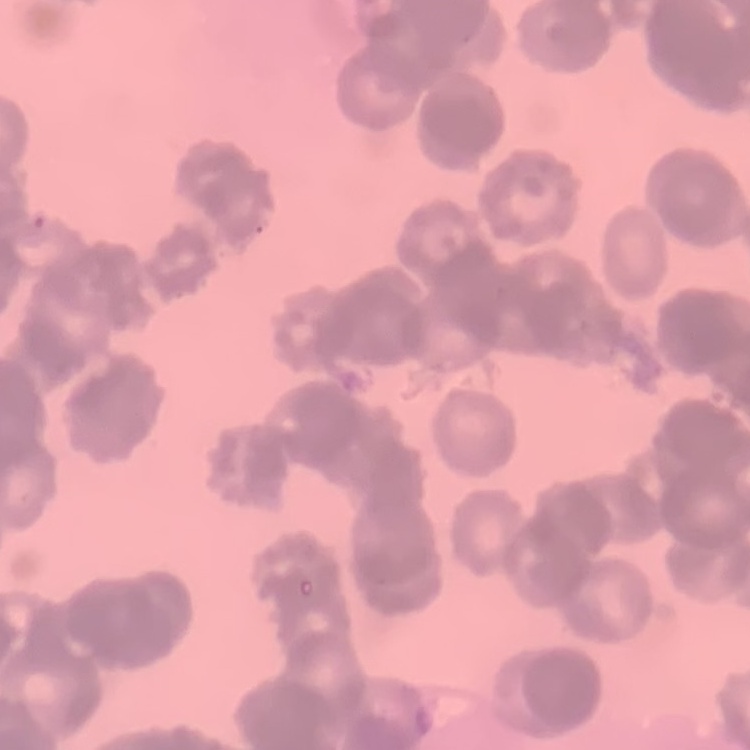

Summary:
  - Red blood cell morphology: rouleaux formation
  - Stain: Field's or Giemsa
  - Preparation: thin blood smear
  - Image type: square crop of a larger photomicrograph